Locate every malaria parasite.
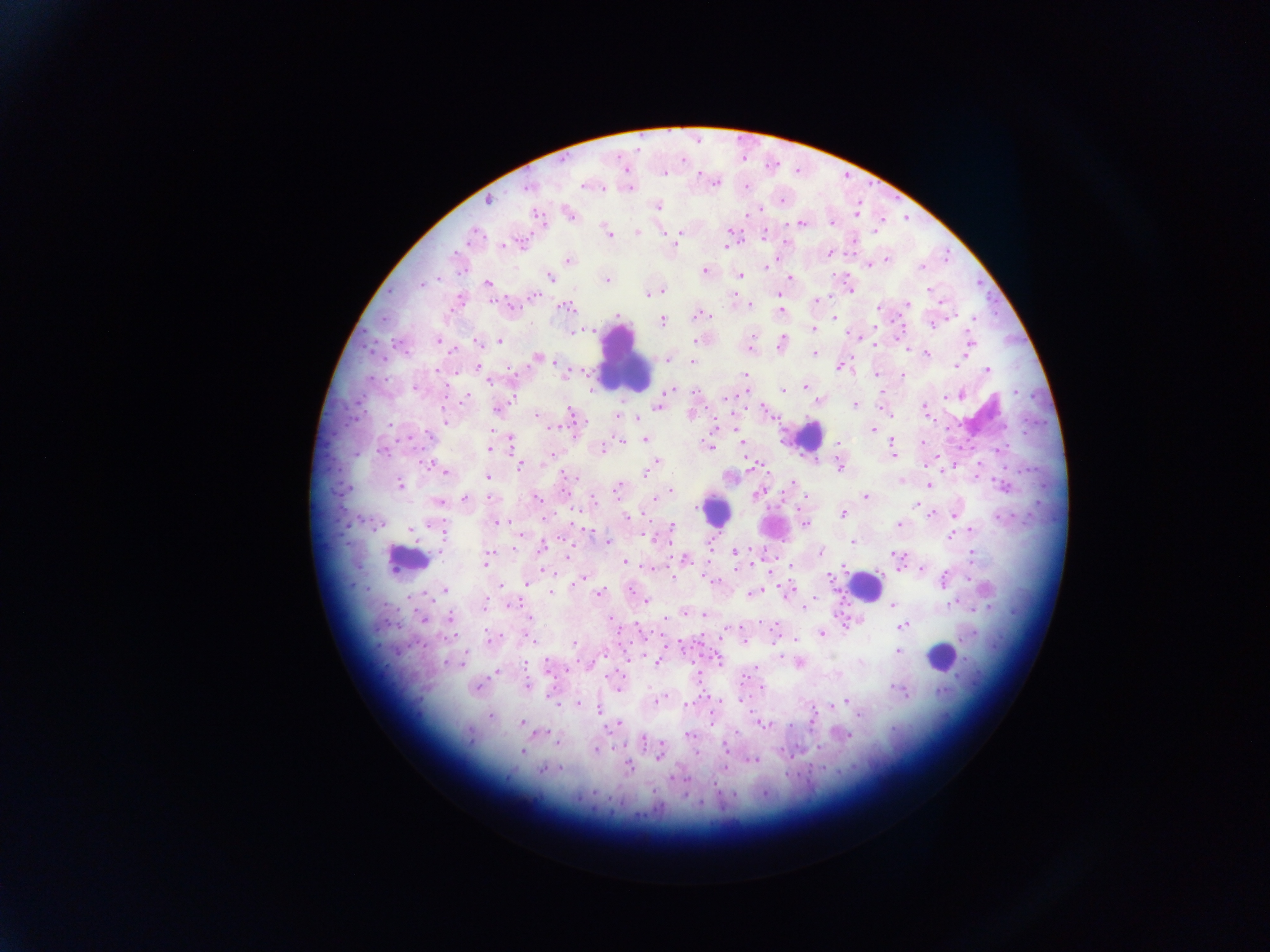

Approximate centers as (x, y) in pixels.
Malaria parasites: (663, 174), (715, 182), (584, 186), (529, 187), (489, 200), (657, 206), (758, 210), (570, 214), (536, 215), (801, 222), (832, 223), (730, 231), (607, 232), (637, 232), (680, 233), (765, 234), (474, 235), (726, 244), (502, 246), (829, 252), (569, 260), (887, 260), (870, 265), (767, 266), (921, 267), (704, 270), (741, 275), (550, 276), (790, 278), (606, 280), (487, 284), (422, 285), (658, 291), (653, 293), (648, 294), (534, 295), (735, 296), (816, 300), (909, 303), (750, 304), (566, 307), (877, 308), (780, 311), (616, 315), (699, 315), (834, 317), (973, 318), (662, 321), (934, 323), (875, 327), (589, 330), (812, 330), (581, 332), (438, 340), (500, 341), (696, 341), (478, 342), (970, 342), (781, 343), (876, 345), (452, 350), (815, 353), (926, 353), (537, 358), (668, 358), (554, 362), (693, 363), (957, 365), (839, 367), (987, 370), (436, 371), (876, 374), (745, 375), (903, 375), (490, 380), (805, 386), (415, 388), (783, 389), (671, 390), (1014, 391), (696, 393), (466, 397), (947, 397), (855, 404), (658, 405), (498, 407), (924, 408), (765, 410), (571, 413), (691, 413), (536, 415), (617, 416), (637, 418), (445, 419), (552, 426), (873, 429), (430, 436), (511, 438), (645, 439), (623, 441), (741, 441), (839, 442), (923, 442), (707, 445), (892, 446), (489, 449), (601, 449), (1001, 449), (383, 451), (893, 452), (655, 463), (428, 464), (520, 466), (651, 467), (839, 467), (445, 472), (646, 473), (566, 475), (487, 477), (901, 481), (792, 483), (400, 484), (929, 485), (1003, 487), (617, 488), (670, 490), (758, 494), (865, 497), (537, 498), (465, 499), (653, 499), (593, 500), (438, 502), (915, 505), (843, 513), (931, 514), (954, 515), (626, 517), (1000, 517), (499, 522), (376, 523), (806, 523), (899, 524), (672, 525), (411, 529), (971, 529), (444, 532), (950, 536), (656, 539), (607, 541), (852, 542), (542, 547), (736, 552), (820, 552), (896, 555), (972, 556), (567, 557), (487, 559), (686, 559), (624, 561), (791, 565), (899, 569), (921, 569), (770, 571), (829, 576), (673, 577), (969, 579), (579, 581), (944, 581), (528, 584), (445, 589), (787, 591), (551, 592), (631, 592), (599, 593), (752, 593), (645, 601), (485, 603), (950, 604), (513, 605), (893, 605), (804, 607), (703, 615), (529, 617), (451, 618), (611, 618), (423, 619), (899, 622), (903, 626), (725, 632), (822, 633), (490, 638), (745, 640), (796, 640), (573, 643), (898, 651), (780, 652), (606, 653), (719, 661), (657, 662), (446, 663), (526, 663), (547, 664), (798, 664), (756, 668), (497, 672), (528, 686), (762, 687), (477, 688), (617, 688), (895, 688), (903, 692), (550, 696), (659, 700), (741, 700), (846, 700), (842, 703), (688, 704), (577, 705), (832, 708), (599, 710), (859, 716), (490, 717), (521, 722), (618, 724), (763, 724), (613, 725), (545, 732), (735, 732), (469, 735), (689, 735), (848, 735), (644, 741), (557, 742), (726, 748), (596, 750), (522, 752), (696, 752), (658, 758), (755, 760), (629, 767), (724, 767), (560, 768), (542, 770), (674, 777), (594, 792), (734, 794), (764, 794).

Leukocyte locations: (624, 361), (808, 435), (715, 511), (407, 560), (863, 586), (940, 656). Single field of view. Collected in Ghana. Thick blood film. Mobile-phone photograph taken through the microscope. Image is 1270×952 pixels.